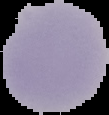
image_size: 109×115 pixels
result: no Plasmodium parasites seen
image_type: segmented cell region on a black background
preparation: thin blood film